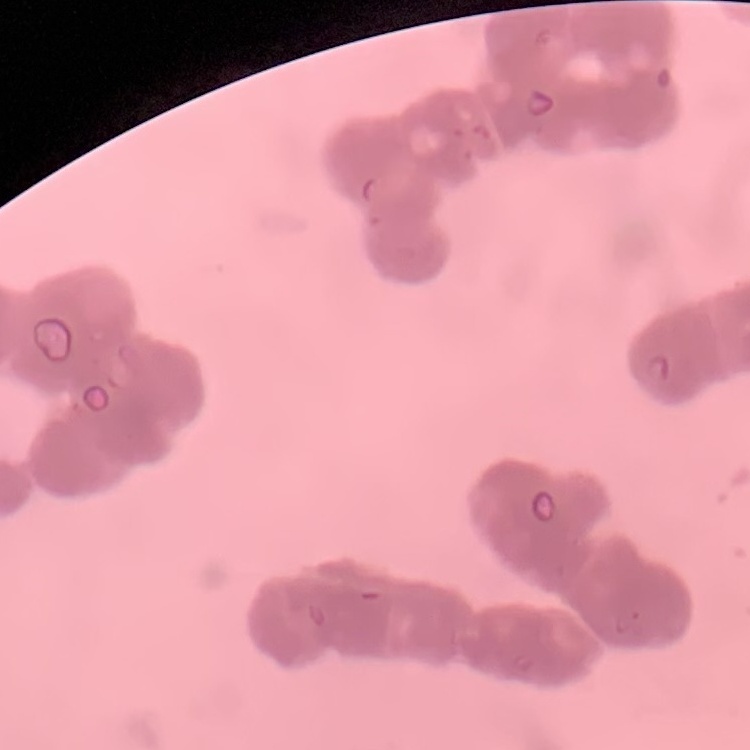
Summary:
  - Erythrocyte morphology: rouleaux formation
  - Image type: one tile cut from a larger photomicrograph
  - Stain: Field's or Giemsa
  - Preparation: thin blood smear